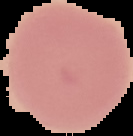

image type = segmented cell region on a black background
result = no malaria parasites detected
preparation = thin blood film
image size = 133×136 pixels